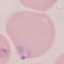 Result: malaria parasites identified. Giemsa-stained preparation. Acquired by smartphone through the microscope eyepiece. Thin smear of blood. Automatically extracted cell patch, resized to 64 × 64 pixels.